Give the preparation type.
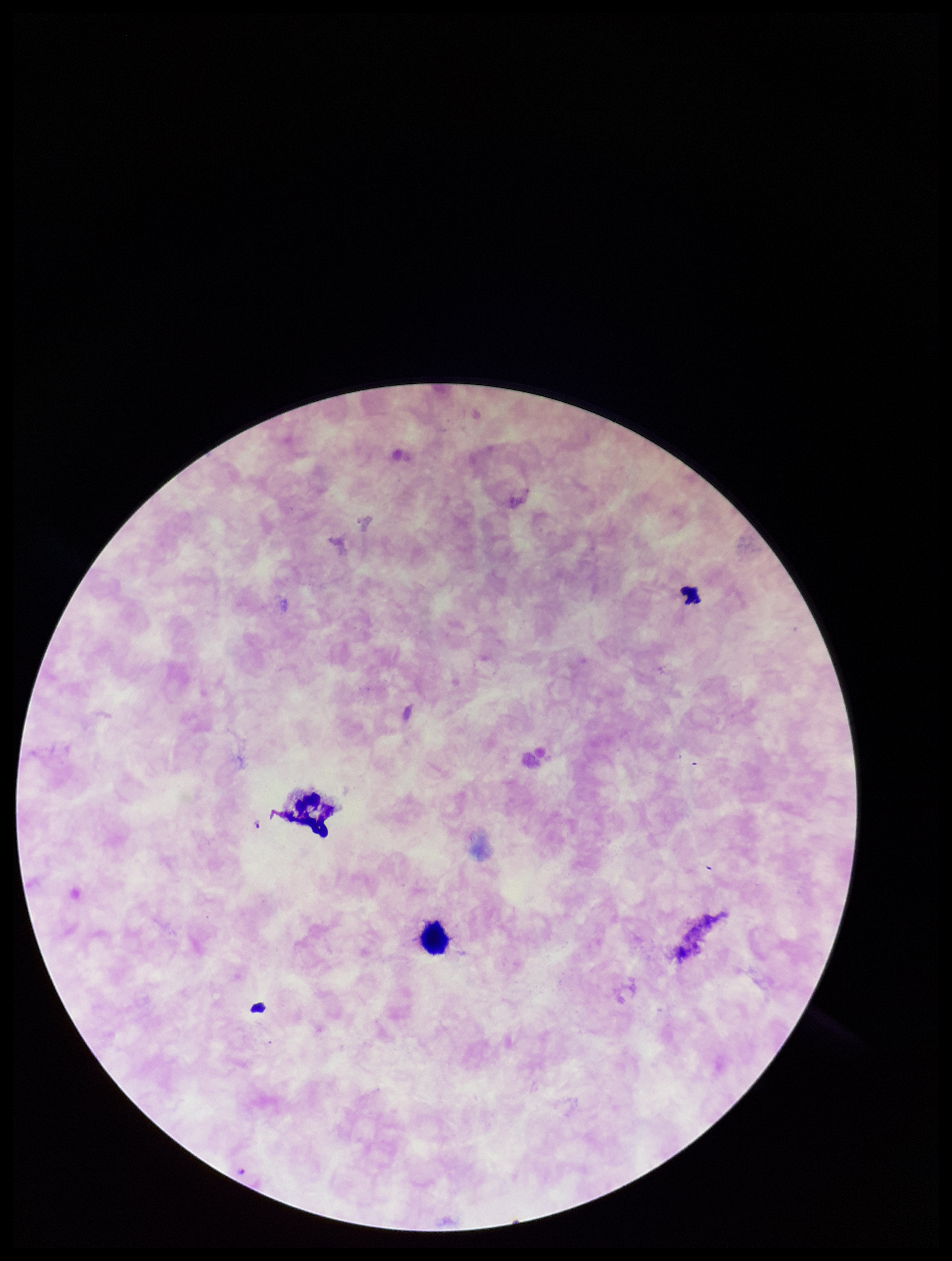
Thick.

Summary:
  - Parasite count: 0
  - Capture: smartphone photograph through the microscope eyepiece
  - Leukocyte count: 2
  - Stain: Giemsa
  - Image size: 952×1261 pixels
  - Species reported for this patient: Plasmodium falciparum
  - Plasmodium parasites: none detected
  - Field of view: one from this slide
  - Patient malaria status: infected